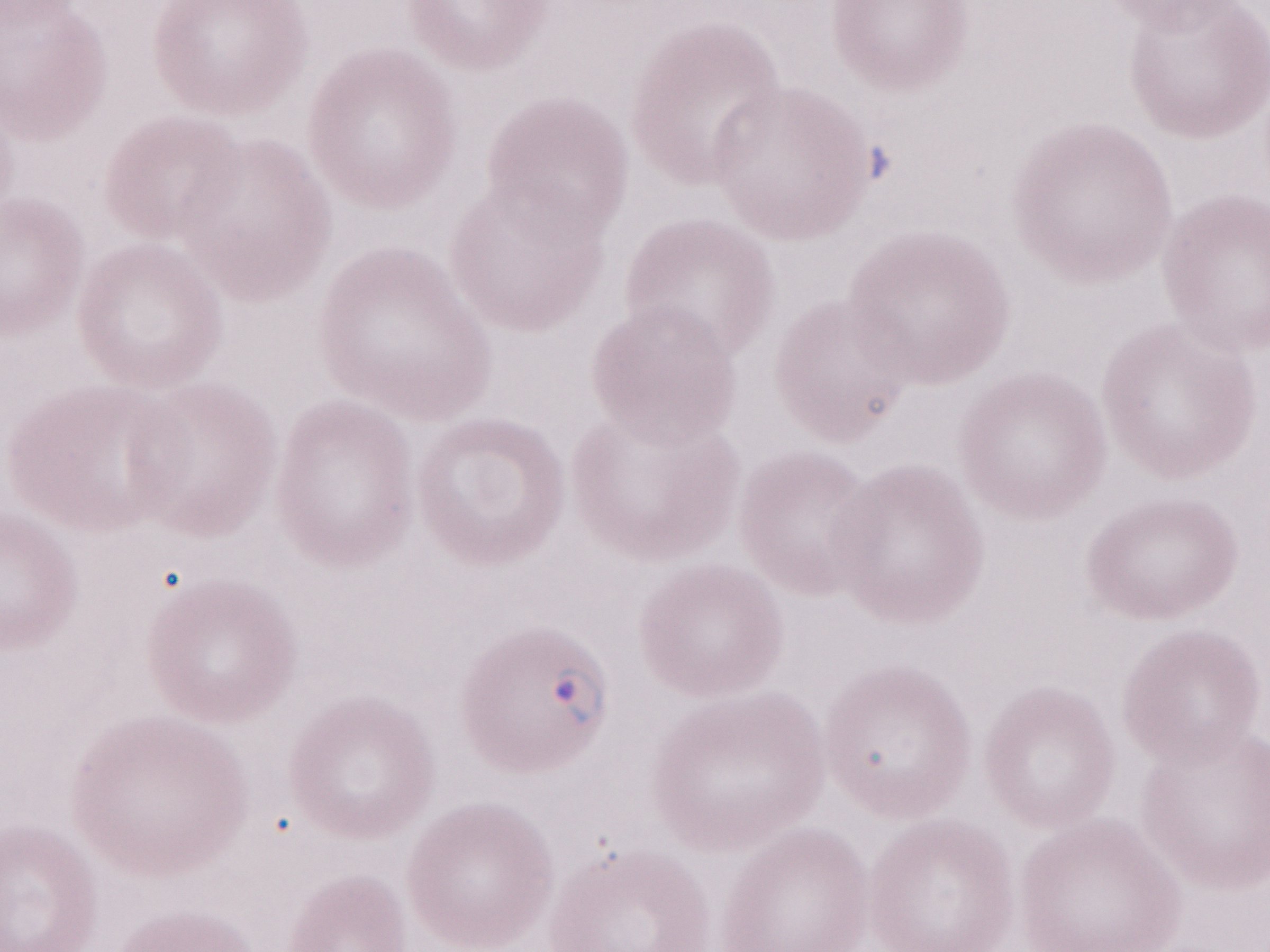
Olympus BX43 microscope, Olympus DP73 camera. Malaria diagnosis (patient-level): positive. Image is 1270×952 pixels. One field of this slide. May-Grünwald-Giemsa (MGG) stain. Thin peripheral-blood smear. 1,000x magnification.